Name the parasite shown.
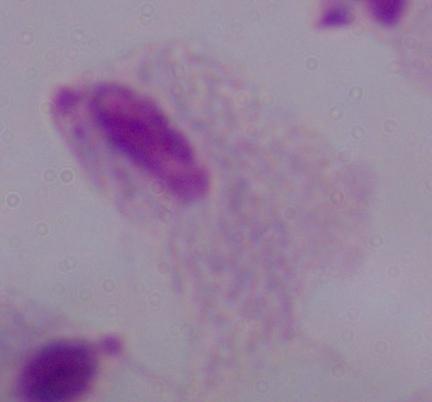
This is a trichomonad.

Summary:
  - Magnification: 1000x
  - Modality: micrograph